Locate and identify every blood parasite.
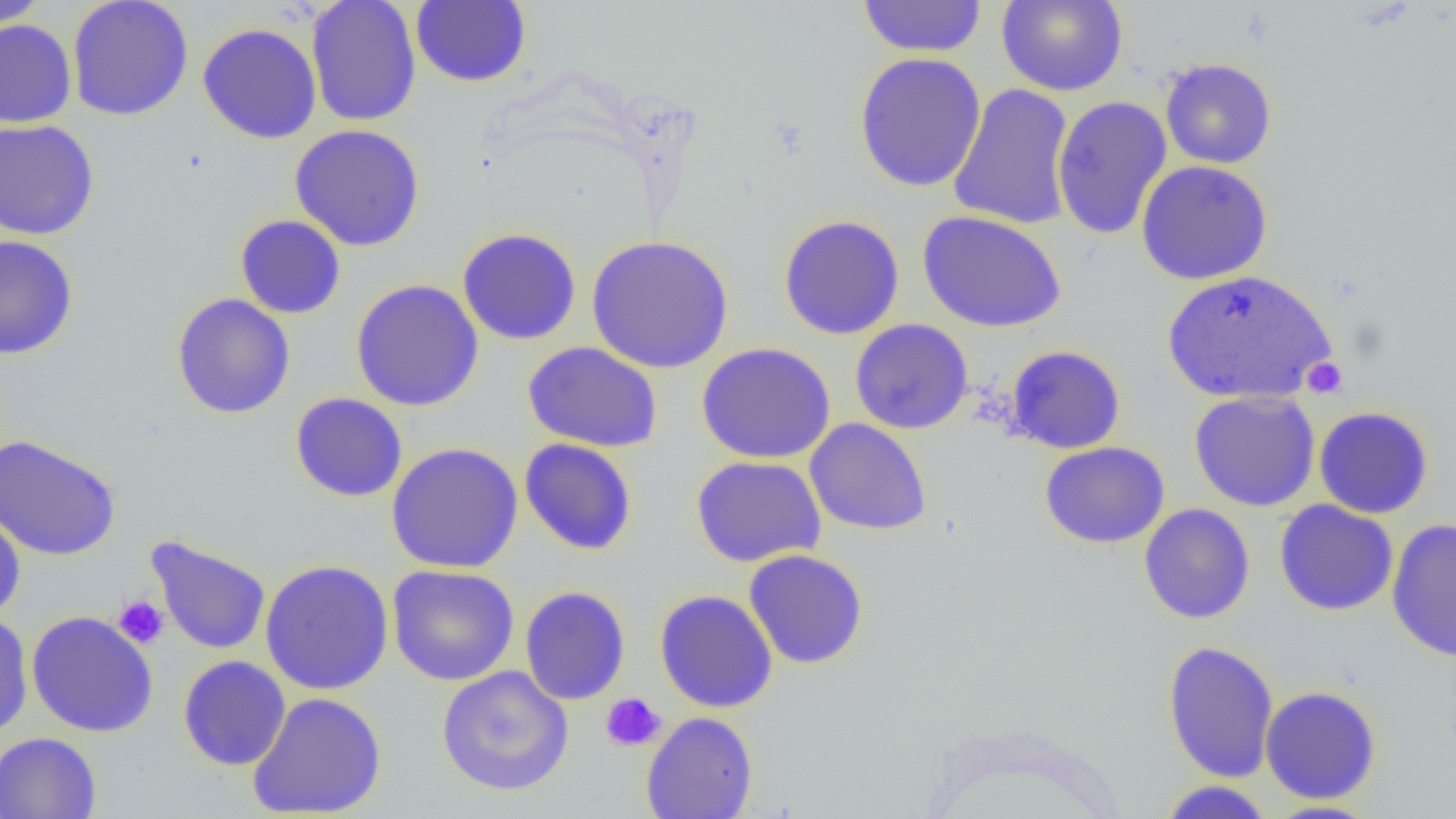
No blood parasites observed.

Approximate bounding boxes as [x1, y1, x2, y2] in pixels. Platelet locations: [1301, 357, 1348, 398], [113, 596, 168, 649], [600, 693, 666, 752]. Uninfected red blood cell locations: [0, 0, 51, 29], [66, 0, 194, 121], [307, 0, 422, 127], [411, 0, 531, 88], [857, 0, 987, 58], [996, 0, 1128, 96], [0, 19, 77, 128], [197, 23, 322, 144], [853, 52, 987, 193], [1160, 57, 1277, 169], [948, 83, 1076, 230], [1052, 95, 1173, 240], [0, 119, 100, 241], [290, 124, 425, 251], [1136, 160, 1273, 284], [917, 211, 1067, 332], [235, 214, 346, 319], [778, 214, 905, 340], [457, 228, 582, 345], [0, 234, 79, 360], [587, 235, 734, 374], [1160, 268, 1338, 404], [350, 279, 484, 412], [171, 293, 296, 419], [849, 319, 974, 434], [522, 341, 662, 453], [696, 342, 836, 464], [1006, 345, 1126, 454], [1189, 390, 1320, 511], [290, 392, 408, 502], [1313, 406, 1434, 519], [805, 418, 932, 536], [0, 434, 121, 560], [519, 438, 637, 555], [1040, 441, 1170, 549], [385, 442, 523, 574], [691, 455, 827, 567], [1274, 500, 1399, 616], [1139, 503, 1255, 624], [0, 507, 26, 622], [1387, 517, 1456, 662], [146, 535, 271, 655], [743, 548, 869, 670], [260, 559, 394, 695], [387, 564, 519, 686], [520, 585, 631, 705], [655, 589, 778, 713], [26, 610, 158, 737], [0, 612, 33, 740], [1162, 640, 1280, 783], [177, 655, 291, 771], [436, 665, 574, 796], [1259, 685, 1382, 804], [247, 691, 387, 819], [641, 711, 759, 819], [0, 732, 101, 819], [1158, 780, 1275, 818], [1262, 800, 1381, 819]. Slide-level diagnosis: negative for blood parasites. Single field of view. Thin blood film. Optical microscopy. Captured at 1000x magnification. Image is 1456×819 pixels.